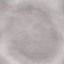

result = negative for malaria parasites
preparation = thin smear
capture = smartphone camera at the microscope eyepiece
stain = Giemsa
image type = cell patch, automatically extracted from a larger field of view and resized to 64 × 64 pixels